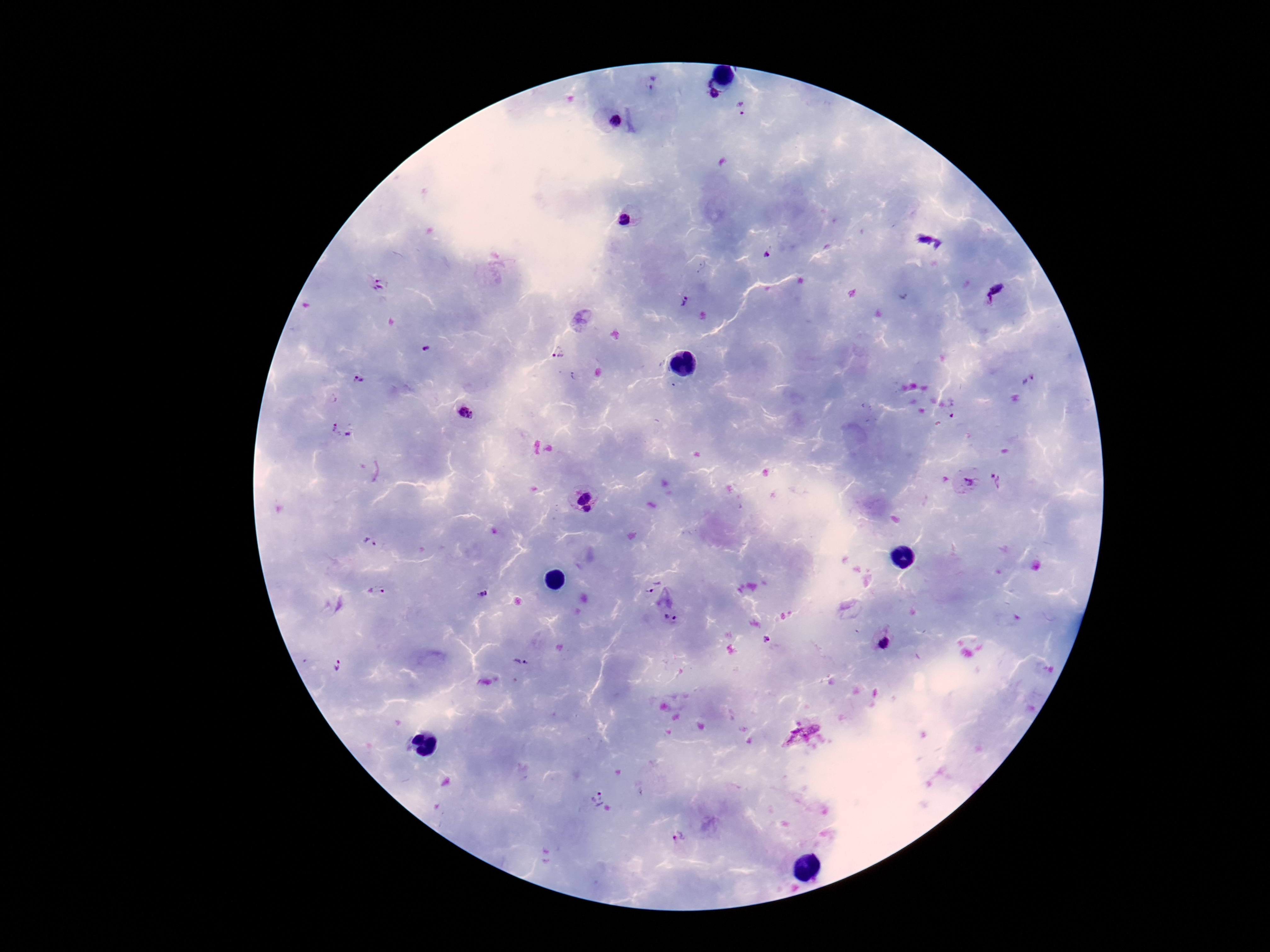
Approximate centers as [x, y] in pixels.
Summary:
  - Plasmodium parasite locations: [653, 83], [708, 83], [714, 94], [741, 109], [615, 123], [624, 220], [930, 241], [767, 254], [377, 286], [995, 292], [684, 303], [426, 350], [558, 354], [1028, 380], [358, 381], [465, 413], [336, 431], [349, 434], [998, 481], [968, 483], [580, 491], [589, 510], [370, 543], [650, 585], [380, 591], [483, 594], [671, 618], [767, 641], [885, 644], [520, 663], [338, 666], [799, 732], [597, 801], [678, 837]
  - Capture: smartphone camera through the microscope eyepiece
  - Preparation: thick blood film
  - Magnification: 100x
  - Stain: Giemsa
  - Image size: 1270×952 pixels
  - Patient malaria status: positive
  - Field of view: single